Report the malaria status of this cell.
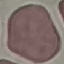

Uninfected.

Photographed with a smartphone camera at the microscope eyepiece. Automatically extracted cell patch, resized to 64 × 64 pixels. Giemsa stain. Thin smear of blood.